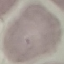

malaria status = uninfected
image type = automatically extracted cell patch, resized to 64 × 64 pixels
capture = smartphone camera at the microscope eyepiece
preparation = thin smear
stain = Giemsa